Identify the blood parasite species.
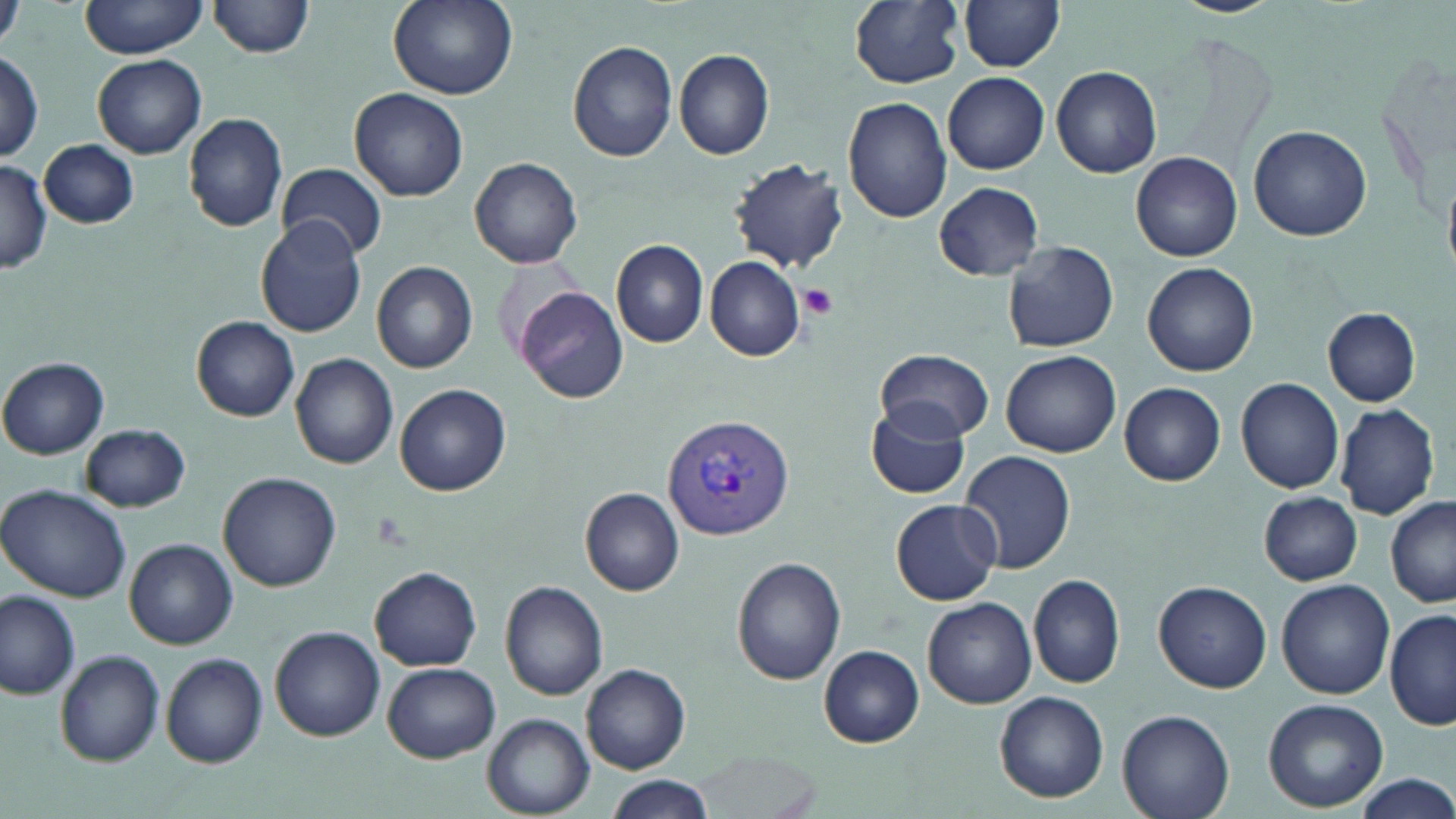
Plasmodium vivax.

Summary:
  - Coordinate format: approximate bounding boxes as (x1,y1)-(x2,y2) corner pairs in pixels
  - Uninfected red blood cell locations: (78,0)-(212,58), (209,0)-(316,58), (387,0)-(518,100), (849,0)-(965,88), (1171,0)-(1284,17), (959,1)-(1065,72), (0,3)-(25,56), (568,40)-(680,162), (674,49)-(774,161), (0,50)-(43,159), (94,54)-(207,159), (1051,65)-(1162,177), (942,71)-(1049,174), (349,87)-(469,202), (843,97)-(953,223), (184,113)-(288,232), (1249,124)-(1371,242), (39,140)-(138,229), (1133,150)-(1244,261), (470,157)-(584,269), (730,157)-(848,273), (0,160)-(51,270), (277,162)-(387,260), (933,182)-(1045,280), (255,217)-(368,338), (611,239)-(709,348), (1003,242)-(1119,352), (704,255)-(806,361), (372,261)-(478,373), (1143,262)-(1259,377), (516,285)-(629,404), (1323,308)-(1421,406), (192,316)-(300,421), (877,348)-(994,441), (1001,350)-(1121,458), (292,353)-(399,470), (0,359)-(109,460), (1234,377)-(1344,494), (1119,382)-(1226,487), (394,384)-(511,496), (865,401)-(972,499), (1335,402)-(1440,519), (80,423)-(190,512), (957,450)-(1076,575), (219,472)-(342,592), (0,484)-(132,603), (580,487)-(684,596), (1260,492)-(1362,585), (890,499)-(1001,604), (1386,499)-(1456,607), (126,539)-(238,649), (732,556)-(848,685), (370,567)-(482,670), (1029,574)-(1125,689), (1277,579)-(1395,699), (500,580)-(608,702), (1153,582)-(1270,692), (0,591)-(80,700), (922,597)-(1037,709), (1385,608)-(1456,732), (271,627)-(386,742), (819,645)-(924,748), (56,649)-(165,766), (162,651)-(268,768), (382,663)-(500,763), (581,663)-(690,773), (994,690)-(1109,803), (1262,698)-(1388,811), (1117,708)-(1235,819), (482,714)-(594,816), (693,749)-(823,817), (1350,773)-(1456,818), (604,775)-(716,818)
  - Plasmodium vivax-infected red blood cell locations: (661,412)-(794,542)
  - Platelet locations: (800,284)-(839,319)
  - Image size: 1456×819 pixels
  - Preparation: thin blood film
  - Magnification: 1000x
  - Stain: May-Grünwald-Giemsa
  - Field of view: one of a larger specimen
  - Modality: optical microscopy